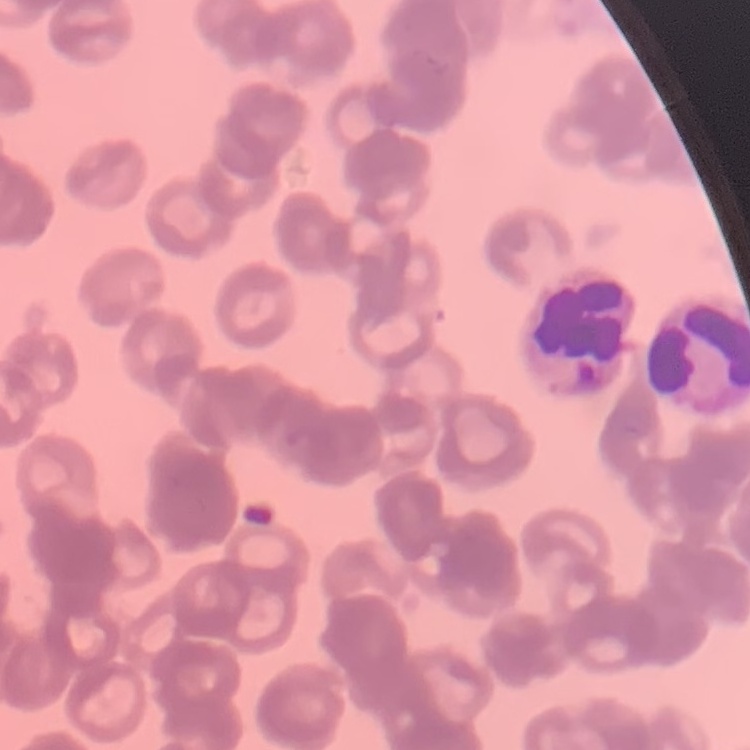 The erythrocytes exhibit rouleaux formation. One tile cut from a larger photomicrograph. Thin peripheral smear. Field's or Giemsa stain.